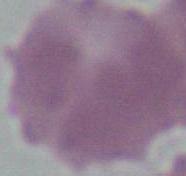

Micrograph. An erythrocyte is seen. Captured at 1000x magnification.